Locate every blood parasite and identify its species.
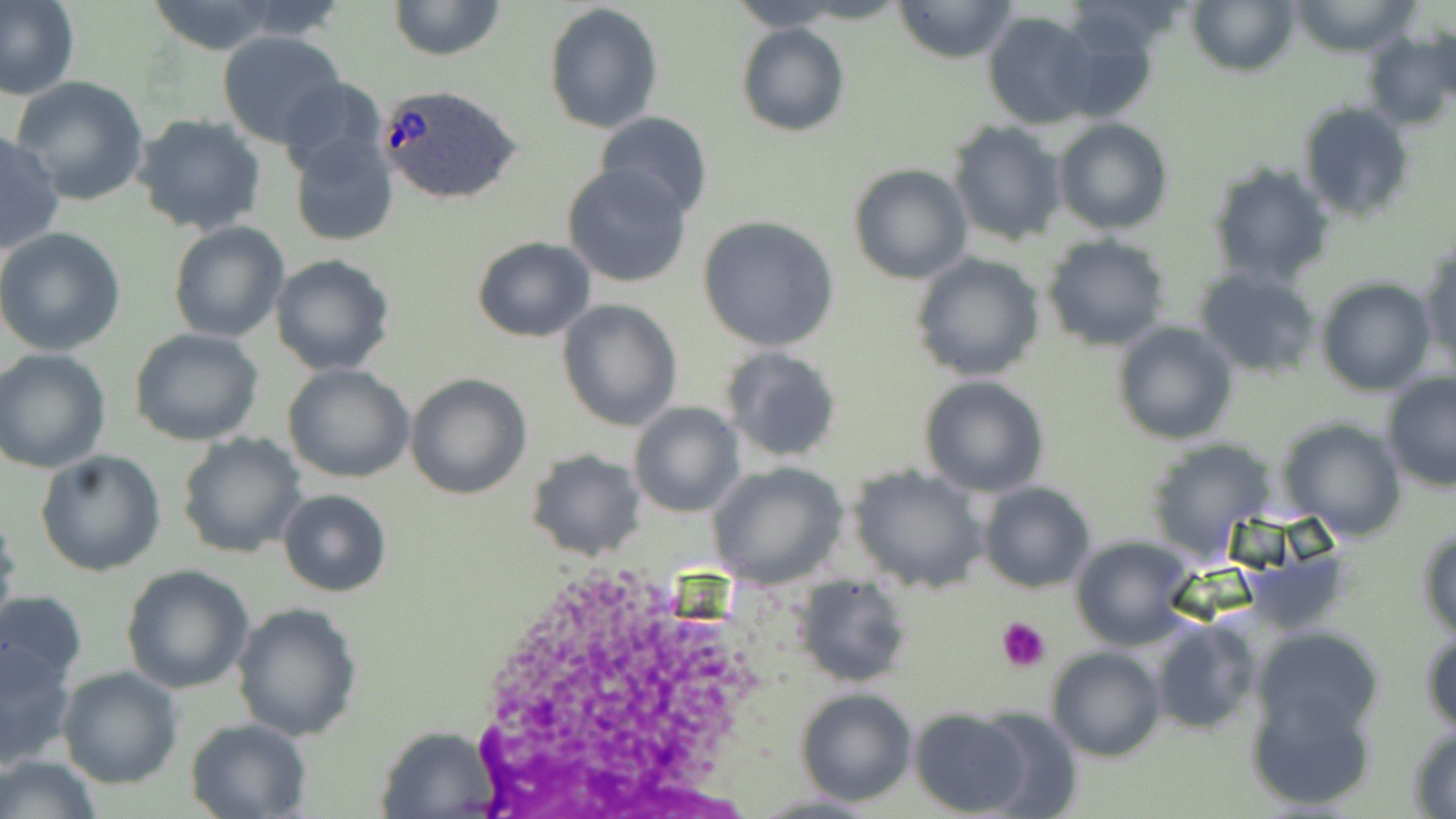

Approximate bounding boxes as (x1,y1)-(x2,y2) corner pairs in pixels.
Plasmodium ovale-infected red blood cells: (378,84)-(522,206).
No Plasmodium falciparum, Plasmodium malariae, Plasmodium vivax, Babesia divergens, or Trypanosoma brucei observed.

Summary:
  - Uninfected red blood cell locations: (0,0)-(81,102), (385,0)-(506,61), (726,0)-(849,31), (892,0)-(1018,64), (1188,0)-(1297,77), (1288,0)-(1423,55), (147,1)-(283,54), (544,2)-(665,136), (983,10)-(1101,129), (735,22)-(851,137), (217,31)-(347,148), (1360,31)-(1455,131), (10,77)-(151,207), (279,78)-(390,184), (1297,101)-(1415,221), (132,113)-(267,236), (594,113)-(712,221), (1055,119)-(1174,235), (948,121)-(1066,247), (0,130)-(65,257), (289,134)-(399,246), (1206,159)-(1336,290), (561,161)-(694,288), (847,162)-(972,285), (697,217)-(841,354), (168,221)-(290,344), (0,227)-(127,357), (1042,235)-(1170,352), (471,237)-(595,342), (1422,242)-(1455,376), (909,252)-(1044,382), (270,254)-(397,376), (1193,267)-(1322,379), (1317,278)-(1437,396), (557,299)-(682,431), (1112,321)-(1237,445), (131,329)-(264,445), (721,347)-(843,462), (0,348)-(111,473), (283,364)-(415,482), (404,373)-(531,499), (1382,374)-(1455,490), (919,376)-(1049,497), (629,402)-(741,515), (1275,415)-(1408,541), (176,433)-(306,559), (1146,438)-(1276,561), (34,449)-(166,577), (526,449)-(646,562), (706,462)-(848,587), (850,466)-(989,593), (978,482)-(1096,594), (279,490)-(391,596), (0,515)-(21,634), (1417,524)-(1456,637), (1069,535)-(1201,650), (120,564)-(255,694), (792,579)-(910,688), (0,590)-(88,689), (231,602)-(364,741), (1149,618)-(1260,735), (1420,624)-(1455,737), (1252,627)-(1385,740), (0,642)-(76,768), (1046,647)-(1165,762), (57,666)-(183,789), (1246,688)-(1377,811), (795,689)-(917,806), (907,708)-(1030,815), (973,708)-(1082,817), (185,718)-(312,818), (373,725)-(504,818), (1407,728)-(1456,816), (0,753)-(104,819)
  - Platelet locations: (997,615)-(1052,671)
  - Slide-level diagnosis: Plasmodium ovale
  - Field of view: one of a larger specimen
  - Image size: 1456×819 pixels
  - Magnification: 1000x
  - Preparation: thin blood smear
  - Stain: May-Grünwald-Giemsa
  - Modality: optical microscopy